Identify the preparation type.
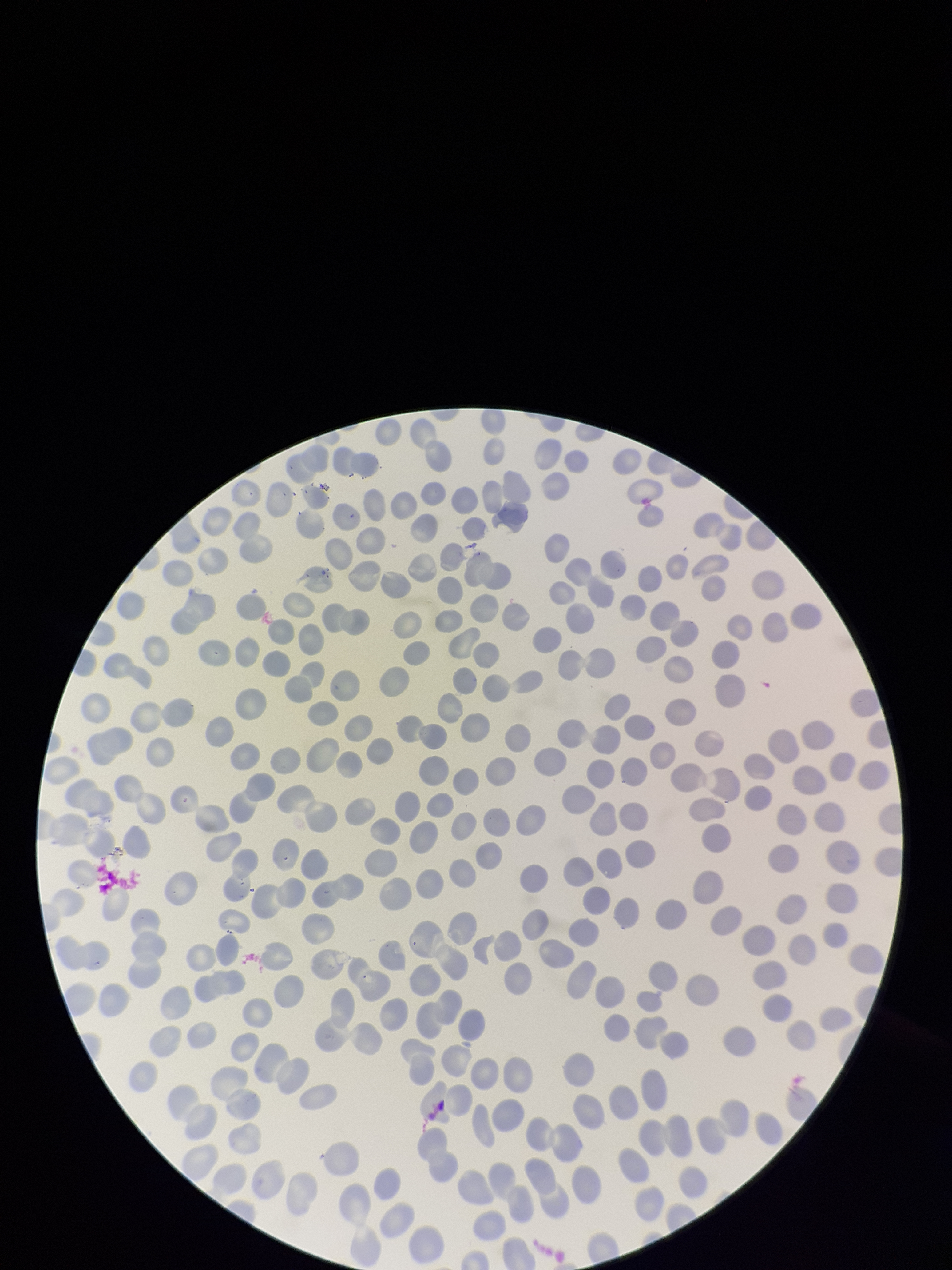
A thin smear.

red blood cell count = 246
field of view = one from this slide
patient malaria status = negative
image size = 952×1270 pixels
stain = Giemsa
parasitized red blood cell count = 0
capture = smartphone photograph through the microscope eyepiece
parasitized red blood cells = none seen